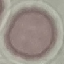

malaria status = uninfected
preparation = thin blood film
stain = Giemsa
capture = smartphone through the microscope eyepiece
image type = automatically extracted cell patch, resized to 64 × 64 pixels